State which parasite is depicted.
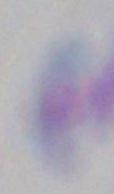
Toxoplasma gondii.

magnification = 1000x
modality = photomicrograph